Identify the parasite.
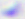
This is Toxoplasma gondii.

400x magnification. Photomicrograph.